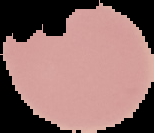

Summary:
  - Image type: segmented cell region with the area outside set to black
  - Image size: 154×133 pixels
  - Malaria status: uninfected
  - Preparation: thin blood smear